State which cell type is depicted.
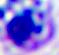

This is a leukocyte.

Photomicrograph. 400x magnification.